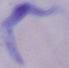
magnification = 1000x
identification = trypanosome
modality = photomicrograph